Evaluate for Plasmodium parasites.
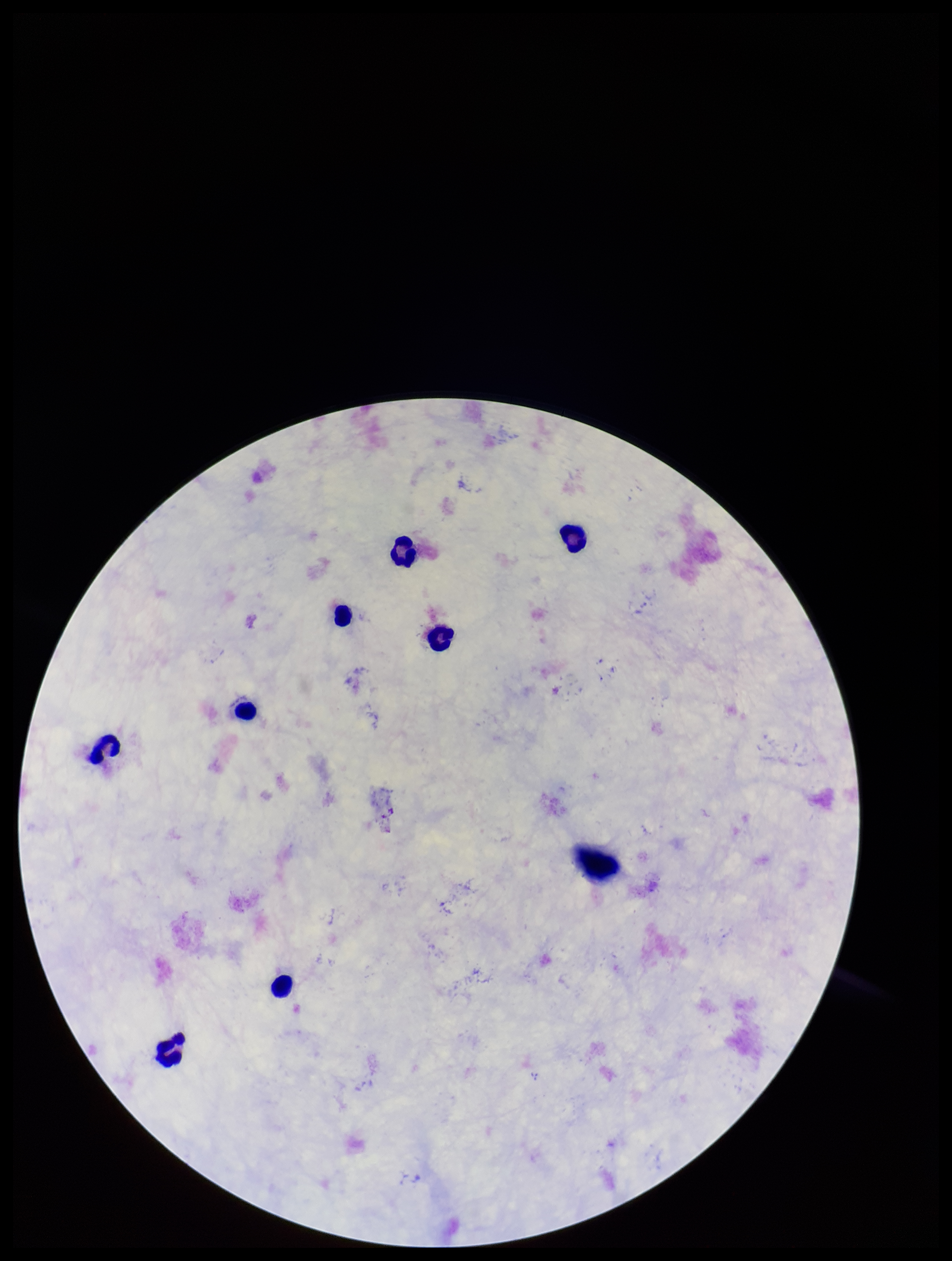
None seen.

Image is 952×1261 pixels. Preparation: thick blood smear. Giemsa stain. Parasite count: 0. Patient malaria status: negative. One field from this slide. Leukocyte count: 8. Photographed through the microscope eyepiece with a smartphone camera.